Locate every malaria parasite and every leukocyte.
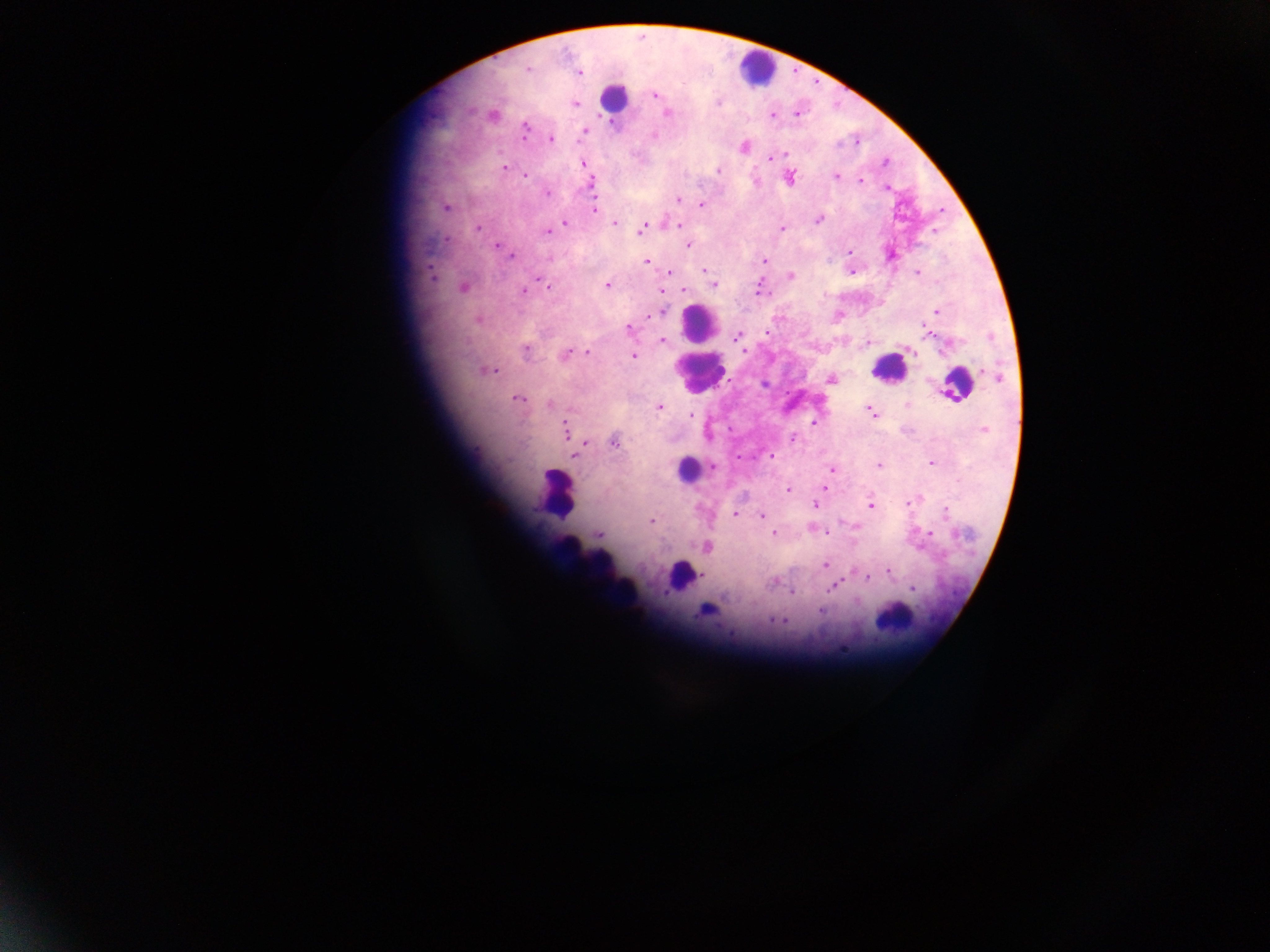

Approximate centers as (x, y) in pixels.
Malaria parasites: (527, 69), (580, 72), (654, 95), (576, 104), (667, 113), (797, 114), (772, 116), (525, 130), (584, 131), (654, 135), (551, 139), (785, 154), (768, 159), (885, 162), (583, 163), (503, 168), (717, 170), (525, 176), (836, 176), (790, 178), (860, 180), (592, 183), (887, 188), (547, 193), (678, 200), (701, 204), (446, 208), (595, 209), (818, 220), (565, 223), (615, 223), (644, 226), (680, 226), (782, 228), (478, 229), (934, 230), (548, 231), (446, 239), (495, 245), (689, 245), (850, 251), (511, 256), (549, 259), (764, 261), (647, 262), (704, 270), (669, 272), (852, 272), (916, 272), (790, 275), (432, 276), (543, 282), (548, 285), (607, 285), (714, 286), (463, 288), (683, 290), (524, 291), (663, 291), (758, 291), (936, 311), (661, 312), (648, 317), (478, 319), (628, 328), (765, 333), (929, 333), (737, 337), (663, 340), (526, 351), (744, 351), (911, 351), (588, 352), (566, 354), (634, 356), (981, 370), (490, 371), (998, 377), (830, 379), (518, 398), (549, 404), (907, 405), (659, 407), (870, 411), (874, 414), (691, 415), (813, 424), (565, 429), (983, 429), (792, 439), (586, 443), (614, 443), (575, 456), (771, 456), (932, 463), (879, 465), (713, 467), (831, 469), (825, 487), (788, 491), (907, 502), (814, 505), (871, 506), (946, 511), (735, 514), (761, 515), (651, 521), (599, 533), (773, 533), (827, 533), (930, 533), (706, 548), (826, 566), (887, 571), (703, 576), (866, 577), (837, 584), (911, 589), (792, 592), (820, 611), (772, 619), (783, 620).
Leukocytes: (757, 69), (613, 97), (700, 325), (889, 369), (699, 375), (956, 385), (687, 469), (556, 493), (567, 544), (595, 567), (680, 576), (628, 587), (894, 618).

{
  "capture": "mobile-phone photograph through a microscope",
  "country": "Ghana",
  "preparation": "thick blood film",
  "field_of_view": "single",
  "image_size": "1270×952 pixels"
}